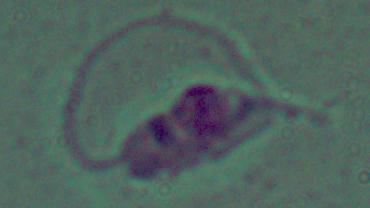

identification = Leishmania
magnification = 1000x
modality = micrograph